Outline each blood parasite and name the species.
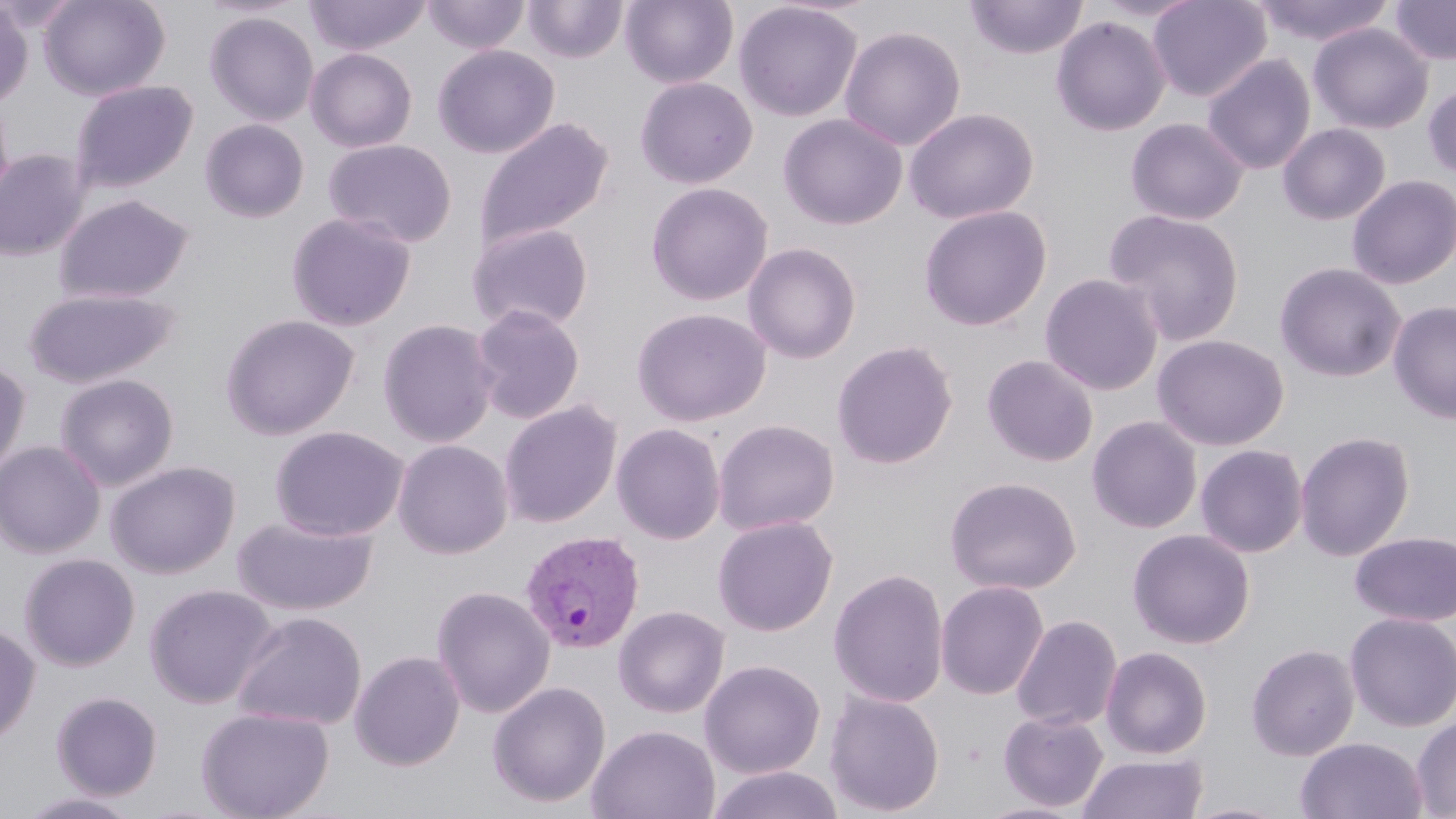
Approximate bounding boxes as named x1/y1/x2/y2 corners in pixels.
Plasmodium vivax-infected red blood cells: (x1=519, y1=530, x2=644, y2=655).
No Plasmodium falciparum, Plasmodium ovale, Plasmodium malariae, Babesia divergens, or Trypanosoma brucei observed.

slide-level diagnosis = Plasmodium vivax
image size = 1456×819 pixels
magnification = 1000x
stain = May-Grünwald-Giemsa
modality = optical microscopy
uninfected red blood cell locations = approximate bounding boxes as named x1/y1/x2/y2 corners in pixels: (x1=38, y1=0, x2=170, y2=100), (x1=304, y1=0, x2=432, y2=56), (x1=422, y1=0, x2=530, y2=54), (x1=620, y1=0, x2=738, y2=88), (x1=964, y1=0, x2=1089, y2=60), (x1=1147, y1=0, x2=1271, y2=102), (x1=1250, y1=0, x2=1395, y2=46), (x1=1389, y1=0, x2=1456, y2=65), (x1=0, y1=1, x2=33, y2=107), (x1=523, y1=1, x2=628, y2=63), (x1=733, y1=1, x2=864, y2=122), (x1=204, y1=11, x2=319, y2=126), (x1=1050, y1=15, x2=1171, y2=136), (x1=1308, y1=22, x2=1433, y2=134), (x1=840, y1=25, x2=966, y2=151), (x1=433, y1=44, x2=559, y2=158), (x1=305, y1=47, x2=417, y2=152), (x1=1202, y1=53, x2=1316, y2=174), (x1=634, y1=76, x2=758, y2=189), (x1=69, y1=80, x2=198, y2=194), (x1=1422, y1=82, x2=1456, y2=180), (x1=0, y1=94, x2=14, y2=211), (x1=904, y1=107, x2=1039, y2=224), (x1=778, y1=113, x2=907, y2=229), (x1=475, y1=117, x2=614, y2=252), (x1=1125, y1=117, x2=1249, y2=225), (x1=199, y1=118, x2=309, y2=222), (x1=1278, y1=123, x2=1391, y2=225), (x1=323, y1=138, x2=457, y2=248), (x1=0, y1=149, x2=89, y2=261), (x1=1346, y1=175, x2=1456, y2=289), (x1=645, y1=182, x2=773, y2=305), (x1=53, y1=193, x2=194, y2=304), (x1=918, y1=204, x2=1052, y2=331), (x1=1103, y1=208, x2=1245, y2=345), (x1=285, y1=212, x2=417, y2=332), (x1=466, y1=222, x2=594, y2=332), (x1=742, y1=242, x2=861, y2=364), (x1=1274, y1=261, x2=1406, y2=383), (x1=1040, y1=273, x2=1164, y2=395), (x1=22, y1=287, x2=179, y2=389), (x1=1388, y1=299, x2=1456, y2=425), (x1=470, y1=304, x2=586, y2=424), (x1=632, y1=307, x2=771, y2=426), (x1=220, y1=314, x2=360, y2=440), (x1=377, y1=319, x2=499, y2=448), (x1=1152, y1=334, x2=1289, y2=451), (x1=831, y1=340, x2=958, y2=469), (x1=982, y1=354, x2=1099, y2=466), (x1=0, y1=362, x2=31, y2=479), (x1=54, y1=373, x2=179, y2=491), (x1=498, y1=400, x2=622, y2=528), (x1=1086, y1=416, x2=1203, y2=534), (x1=713, y1=419, x2=840, y2=536), (x1=611, y1=423, x2=726, y2=545), (x1=270, y1=425, x2=409, y2=541), (x1=1295, y1=431, x2=1415, y2=561), (x1=392, y1=439, x2=513, y2=558), (x1=0, y1=441, x2=105, y2=558), (x1=1195, y1=444, x2=1308, y2=557), (x1=106, y1=460, x2=240, y2=579), (x1=944, y1=475, x2=1082, y2=595), (x1=712, y1=515, x2=838, y2=636), (x1=232, y1=516, x2=378, y2=617), (x1=1127, y1=528, x2=1255, y2=649), (x1=1350, y1=531, x2=1456, y2=626), (x1=18, y1=553, x2=140, y2=672), (x1=828, y1=568, x2=949, y2=708), (x1=935, y1=580, x2=1049, y2=700), (x1=144, y1=583, x2=277, y2=709), (x1=431, y1=586, x2=556, y2=718), (x1=613, y1=605, x2=730, y2=718), (x1=231, y1=611, x2=367, y2=731), (x1=1344, y1=612, x2=1456, y2=732), (x1=1011, y1=614, x2=1122, y2=731), (x1=0, y1=623, x2=40, y2=748), (x1=1246, y1=643, x2=1360, y2=761), (x1=1101, y1=646, x2=1212, y2=759), (x1=349, y1=650, x2=465, y2=771), (x1=699, y1=659, x2=826, y2=779), (x1=487, y1=681, x2=611, y2=808), (x1=825, y1=690, x2=945, y2=816), (x1=51, y1=691, x2=163, y2=800), (x1=195, y1=706, x2=335, y2=819), (x1=998, y1=710, x2=1109, y2=812), (x1=1411, y1=714, x2=1456, y2=818), (x1=586, y1=724, x2=721, y2=819), (x1=1295, y1=736, x2=1429, y2=819), (x1=1077, y1=752, x2=1208, y2=819), (x1=706, y1=765, x2=845, y2=819), (x1=16, y1=790, x2=144, y2=818), (x1=974, y1=801, x2=1088, y2=819), (x1=1182, y1=801, x2=1296, y2=819)
preparation = thin blood smear
field of view = one of a larger specimen